Locate and identify every blood parasite.
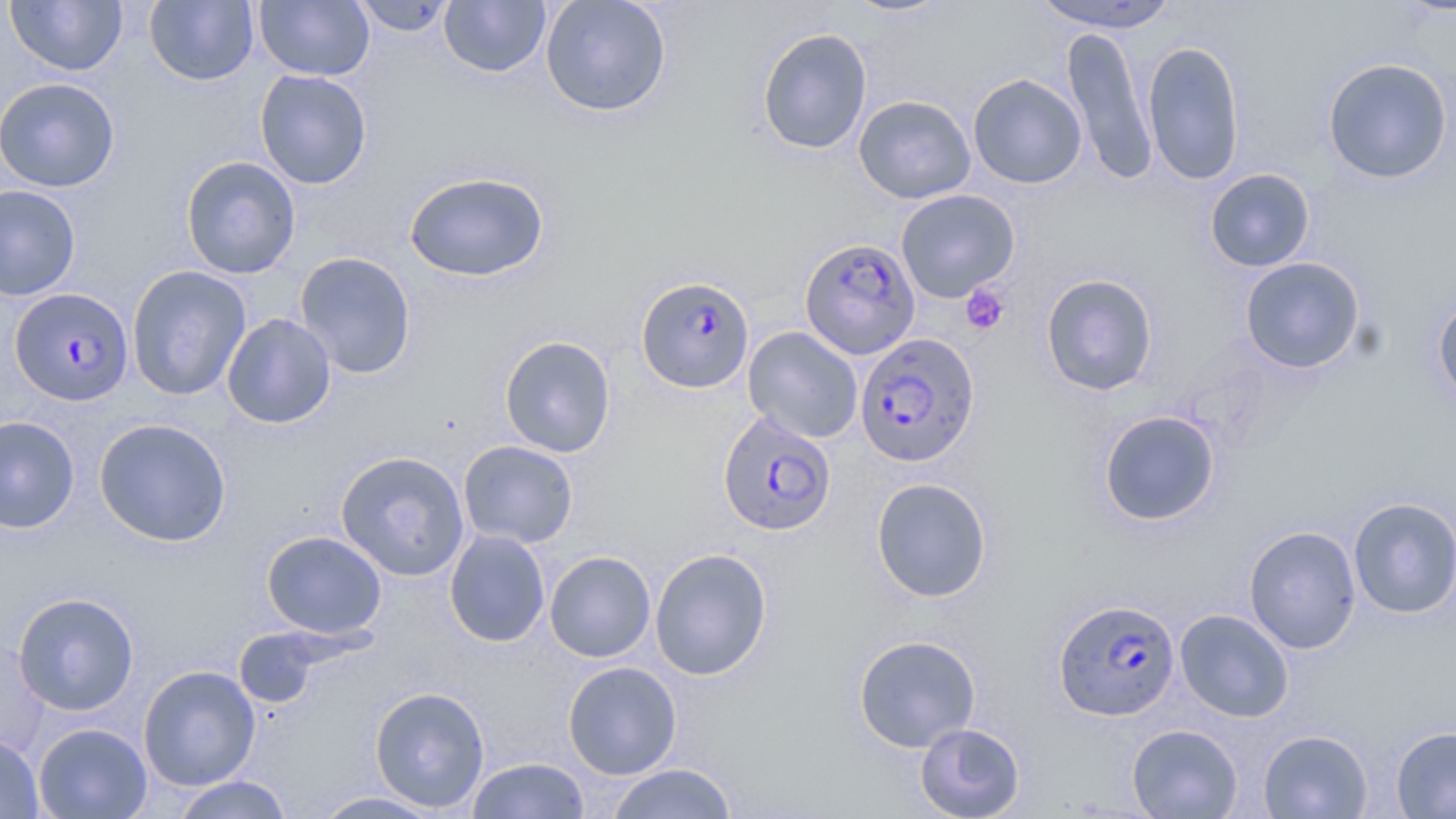
Approximate bounding boxes as named x1/y1/x2/y2 corners in pixels.
Plasmodium falciparum-infected red blood cells: (x1=799, y1=237, x2=921, y2=359), (x1=635, y1=276, x2=755, y2=392), (x1=10, y1=287, x2=134, y2=405), (x1=854, y1=333, x2=980, y2=468), (x1=717, y1=411, x2=836, y2=536), (x1=1053, y1=598, x2=1181, y2=721).
No Plasmodium ovale, Plasmodium malariae, Plasmodium vivax, Babesia divergens, or Trypanosoma brucei observed.

slide-level diagnosis = Plasmodium falciparum
modality = light microscopy
preparation = thin blood film
stain = May-Grünwald-Giemsa
field of view = single
magnification = 1000x
platelet locations = approximate bounding boxes as named x1/y1/x2/y2 corners in pixels: (x1=960, y1=284, x2=1010, y2=335)
uninfected red blood cell locations = approximate bounding boxes as named x1/y1/x2/y2 corners in pixels: (x1=6, y1=0, x2=128, y2=76), (x1=145, y1=0, x2=259, y2=86), (x1=254, y1=0, x2=375, y2=81), (x1=350, y1=0, x2=457, y2=37), (x1=539, y1=0, x2=672, y2=118), (x1=840, y1=0, x2=956, y2=18), (x1=1031, y1=0, x2=1183, y2=33), (x1=439, y1=1, x2=552, y2=78), (x1=1061, y1=25, x2=1158, y2=186), (x1=756, y1=27, x2=872, y2=155), (x1=1142, y1=40, x2=1246, y2=185), (x1=1322, y1=57, x2=1453, y2=184), (x1=254, y1=69, x2=373, y2=189), (x1=967, y1=73, x2=1087, y2=189), (x1=0, y1=78, x2=121, y2=192), (x1=854, y1=95, x2=976, y2=204), (x1=180, y1=156, x2=301, y2=279), (x1=1205, y1=168, x2=1316, y2=273), (x1=404, y1=171, x2=549, y2=282), (x1=0, y1=185, x2=82, y2=301), (x1=896, y1=189, x2=1020, y2=303), (x1=294, y1=251, x2=417, y2=379), (x1=1239, y1=257, x2=1366, y2=374), (x1=127, y1=265, x2=251, y2=400), (x1=1040, y1=273, x2=1159, y2=396), (x1=1431, y1=292, x2=1456, y2=410), (x1=222, y1=313, x2=336, y2=429), (x1=743, y1=326, x2=864, y2=443), (x1=499, y1=336, x2=616, y2=458), (x1=1097, y1=410, x2=1221, y2=527), (x1=0, y1=414, x2=80, y2=534), (x1=93, y1=417, x2=232, y2=546), (x1=458, y1=440, x2=579, y2=549), (x1=335, y1=450, x2=470, y2=582), (x1=871, y1=477, x2=992, y2=602), (x1=1347, y1=496, x2=1456, y2=619), (x1=1243, y1=525, x2=1362, y2=654), (x1=444, y1=529, x2=550, y2=648), (x1=261, y1=530, x2=387, y2=640), (x1=649, y1=548, x2=773, y2=680), (x1=544, y1=551, x2=656, y2=662), (x1=13, y1=592, x2=140, y2=716), (x1=1175, y1=609, x2=1294, y2=722), (x1=233, y1=629, x2=334, y2=710), (x1=853, y1=634, x2=981, y2=752), (x1=562, y1=661, x2=682, y2=779), (x1=138, y1=665, x2=261, y2=790), (x1=370, y1=686, x2=490, y2=813), (x1=914, y1=722, x2=1026, y2=818), (x1=33, y1=723, x2=153, y2=818), (x1=1126, y1=724, x2=1243, y2=818), (x1=1390, y1=725, x2=1456, y2=818), (x1=1258, y1=729, x2=1373, y2=818), (x1=0, y1=733, x2=45, y2=819), (x1=466, y1=757, x2=590, y2=818), (x1=605, y1=763, x2=738, y2=819), (x1=169, y1=775, x2=295, y2=819), (x1=310, y1=790, x2=449, y2=818)
image size = 1456×819 pixels